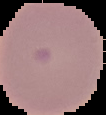
Malaria status: uninfected. From a thin blood smear. Image is 106×115 pixels. Cell region segmented out of the field of view; the surrounding area is masked to black.